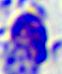

Photomicrograph. A white blood cell is seen. Captured at 400x magnification.